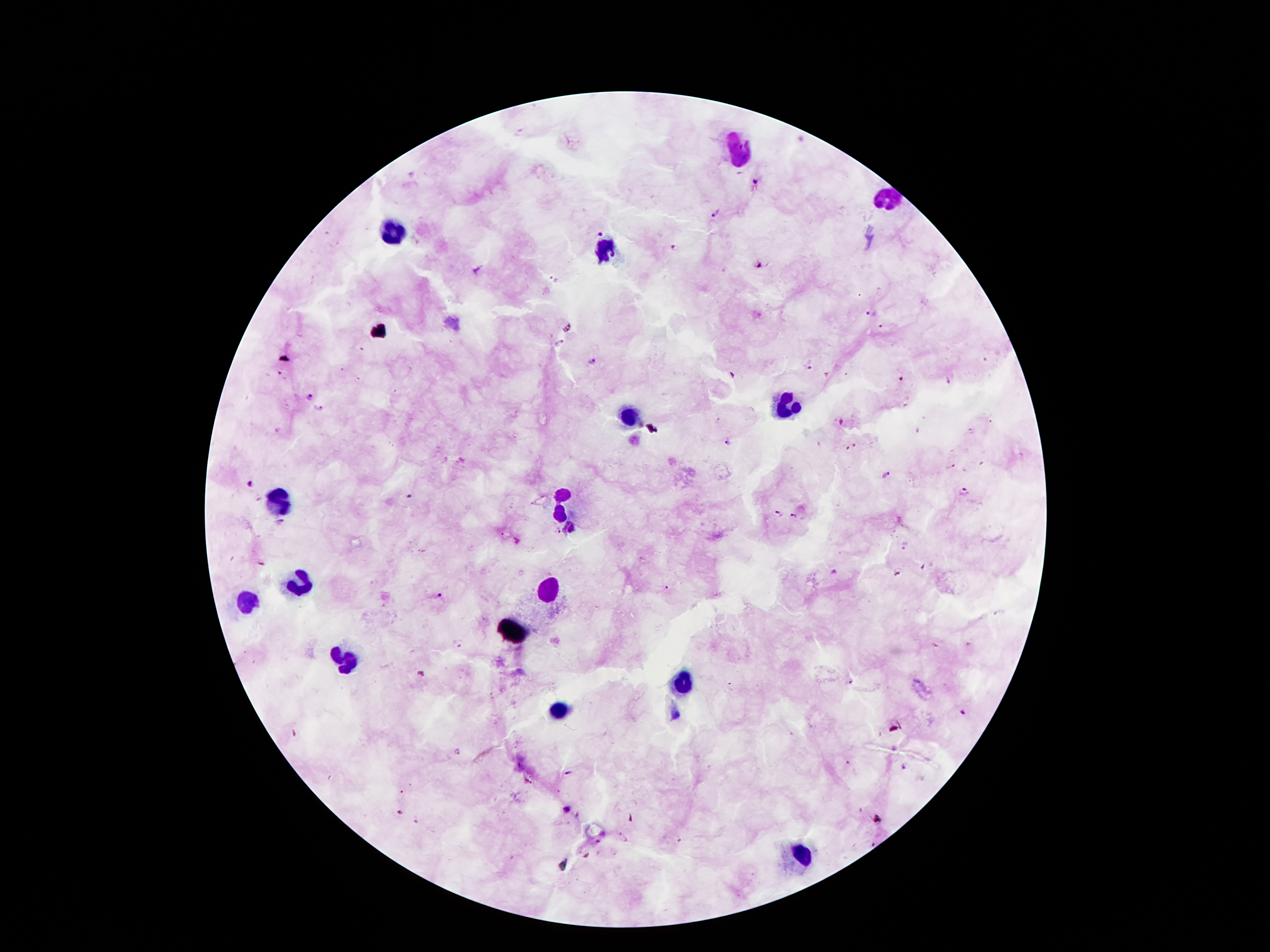 Approximate object centers, in pixels from the top-left corner. Malaria parasite locations: (x=757, y=181), (x=715, y=212), (x=599, y=232), (x=674, y=248), (x=757, y=263), (x=555, y=278), (x=870, y=314), (x=880, y=326), (x=561, y=345), (x=590, y=361), (x=807, y=368), (x=899, y=381), (x=948, y=381), (x=310, y=395), (x=320, y=408), (x=842, y=423), (x=971, y=431), (x=728, y=442), (x=855, y=445), (x=847, y=448), (x=950, y=467), (x=886, y=475), (x=247, y=484), (x=963, y=491), (x=410, y=498), (x=779, y=512), (x=794, y=516), (x=281, y=523), (x=557, y=531), (x=905, y=546), (x=665, y=588), (x=436, y=595), (x=458, y=644), (x=850, y=682), (x=961, y=713), (x=456, y=753), (x=906, y=767), (x=569, y=773). Leukocyte locations: (x=739, y=150), (x=891, y=196), (x=394, y=231), (x=604, y=252), (x=786, y=408), (x=630, y=418), (x=278, y=499), (x=567, y=507), (x=301, y=582), (x=546, y=592), (x=250, y=601), (x=681, y=683), (x=558, y=711), (x=802, y=858). Giemsa stain. Image is 1270×952 pixels. Patient malaria status: infected with Plasmodium falciparum. Photographed through the microscope eyepiece with a smartphone camera. Thick peripheral-blood smear. Single field of view. 100x magnification.